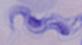

Summary:
  - Magnification: 1000x
  - Identification: trypanosome
  - Modality: photomicrograph